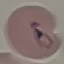
Summary:
  - Malaria status: parasitized
  - Capture: smartphone through the microscope eyepiece
  - Image type: automatically extracted cell patch, resized to 64 × 64 pixels
  - Preparation: thin blood film
  - Stain: Giemsa